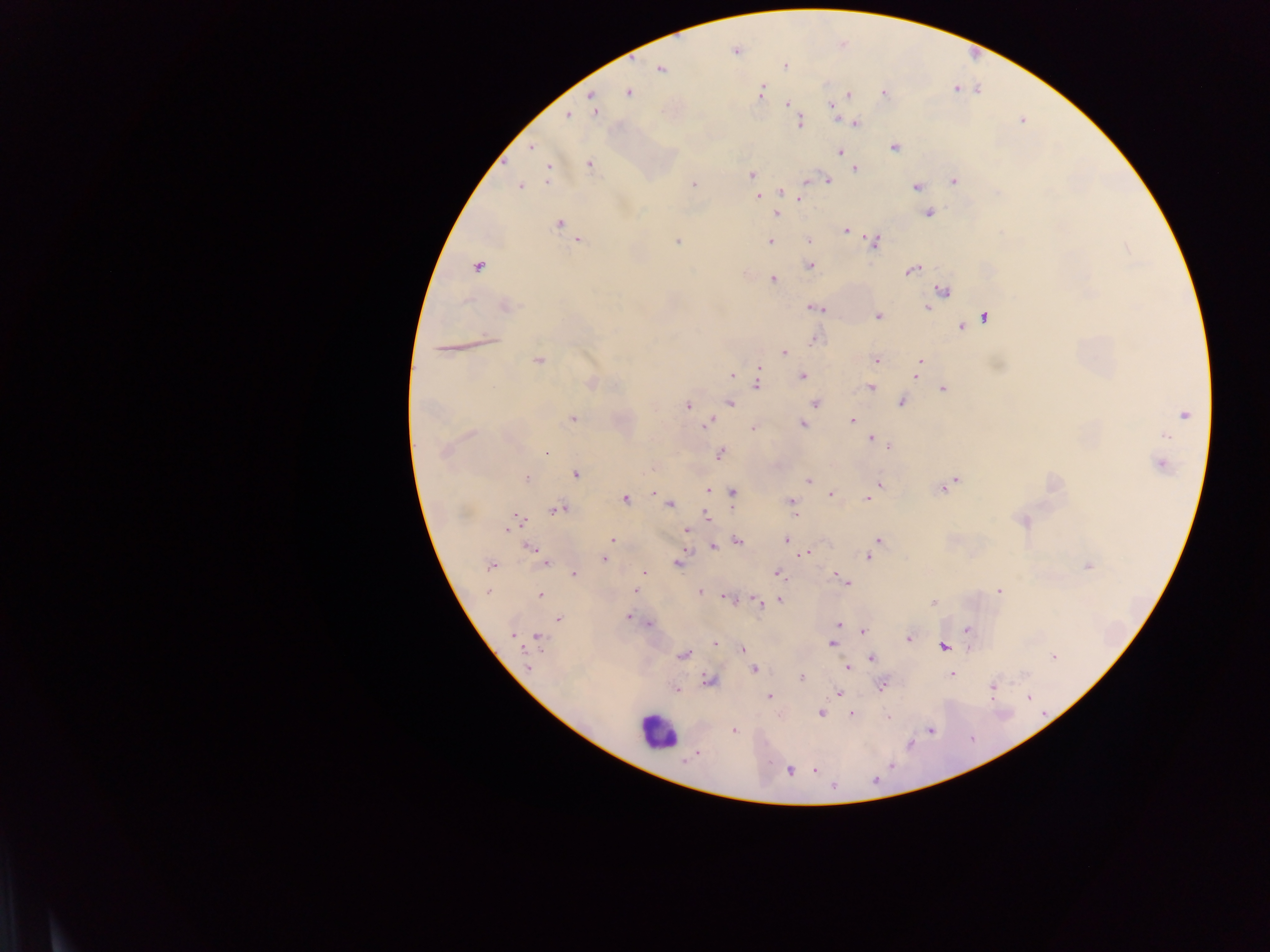
Approximate centers as (x, y) in pixels.
Summary:
  - Malaria parasite locations: (736, 51), (786, 65), (661, 69), (761, 92), (628, 93), (884, 93), (849, 95), (592, 96), (788, 103), (831, 106), (596, 111), (568, 116), (800, 122), (855, 123), (531, 147), (894, 147), (839, 151), (589, 164), (855, 168), (548, 172), (752, 176), (828, 181), (954, 181), (753, 182), (807, 182), (693, 184), (520, 186), (917, 186), (783, 192), (757, 197), (799, 197), (928, 213), (776, 214), (559, 223), (845, 230), (579, 240), (678, 241), (771, 241), (809, 241), (874, 242), (809, 265), (478, 266), (912, 270), (773, 280), (943, 291), (506, 306), (815, 308), (926, 308), (878, 316), (984, 318), (961, 327), (490, 340), (815, 341), (784, 352), (538, 360), (876, 360), (919, 363), (758, 369), (917, 373), (732, 375), (802, 376), (592, 383), (758, 383), (870, 388), (943, 389), (902, 402), (729, 403), (815, 403), (687, 406), (1185, 414), (572, 419), (851, 420), (707, 423), (802, 425), (754, 428), (471, 434), (1166, 436), (871, 438), (889, 446), (445, 452), (546, 452), (720, 454), (1161, 464), (576, 474), (527, 478), (809, 481), (954, 481), (879, 484), (942, 487), (708, 490), (653, 493), (733, 493), (830, 494), (625, 499), (867, 499), (791, 501), (670, 505), (558, 509), (795, 515), (707, 516), (516, 521), (1024, 521), (508, 529), (686, 531), (787, 539), (612, 540), (878, 540), (737, 541), (713, 546), (530, 548), (805, 554), (536, 556), (868, 556), (604, 559), (544, 562), (678, 563), (491, 565), (1088, 566), (644, 572), (574, 574), (778, 574), (836, 576), (845, 582), (635, 591), (999, 591), (488, 592), (700, 592), (541, 595), (728, 599), (780, 601), (758, 602), (933, 603), (628, 617), (558, 619), (839, 624), (648, 625), (967, 629), (863, 632), (513, 635), (538, 638), (908, 638), (715, 643), (832, 643), (944, 646), (743, 649), (684, 655), (1053, 657), (871, 658), (527, 667), (848, 668), (753, 669), (951, 674), (801, 677), (709, 680), (882, 686), (993, 687), (676, 689), (839, 693), (770, 696), (1028, 697), (821, 713), (851, 713), (889, 717), (931, 729), (734, 730), (696, 753), (815, 770), (791, 772), (833, 786)
  - Leukocyte locations: (655, 730)
  - Field of view: single
  - Country: Ghana
  - Image size: 1270×952 pixels
  - Capture: mobile-phone photograph through a microscope
  - Preparation: thick blood film